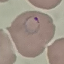
Malaria status: parasitized. Cell patch, automatically extracted from a larger field of view and resized to 64 × 64 pixels. Thin smear of blood. Photographed with a smartphone camera at the microscope eyepiece. Giemsa-stained preparation.